Identify the parasite.
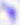

This is Toxoplasma gondii.

Summary:
  - Magnification: 400x
  - Modality: micrograph